Classify this cell by malaria status.
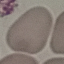
It is uninfected.

Summary:
  - Image type: automatically extracted cell patch, resized to 64 × 64 pixels
  - Stain: Giemsa
  - Capture: smartphone through the microscope eyepiece
  - Preparation: thin blood film